Assess this cell for malaria.
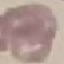

Uninfected.

Acquired by smartphone through the microscope eyepiece. Thin smear of blood. Automatically extracted cell patch, resized to 64 × 64 pixels. Giemsa stain.